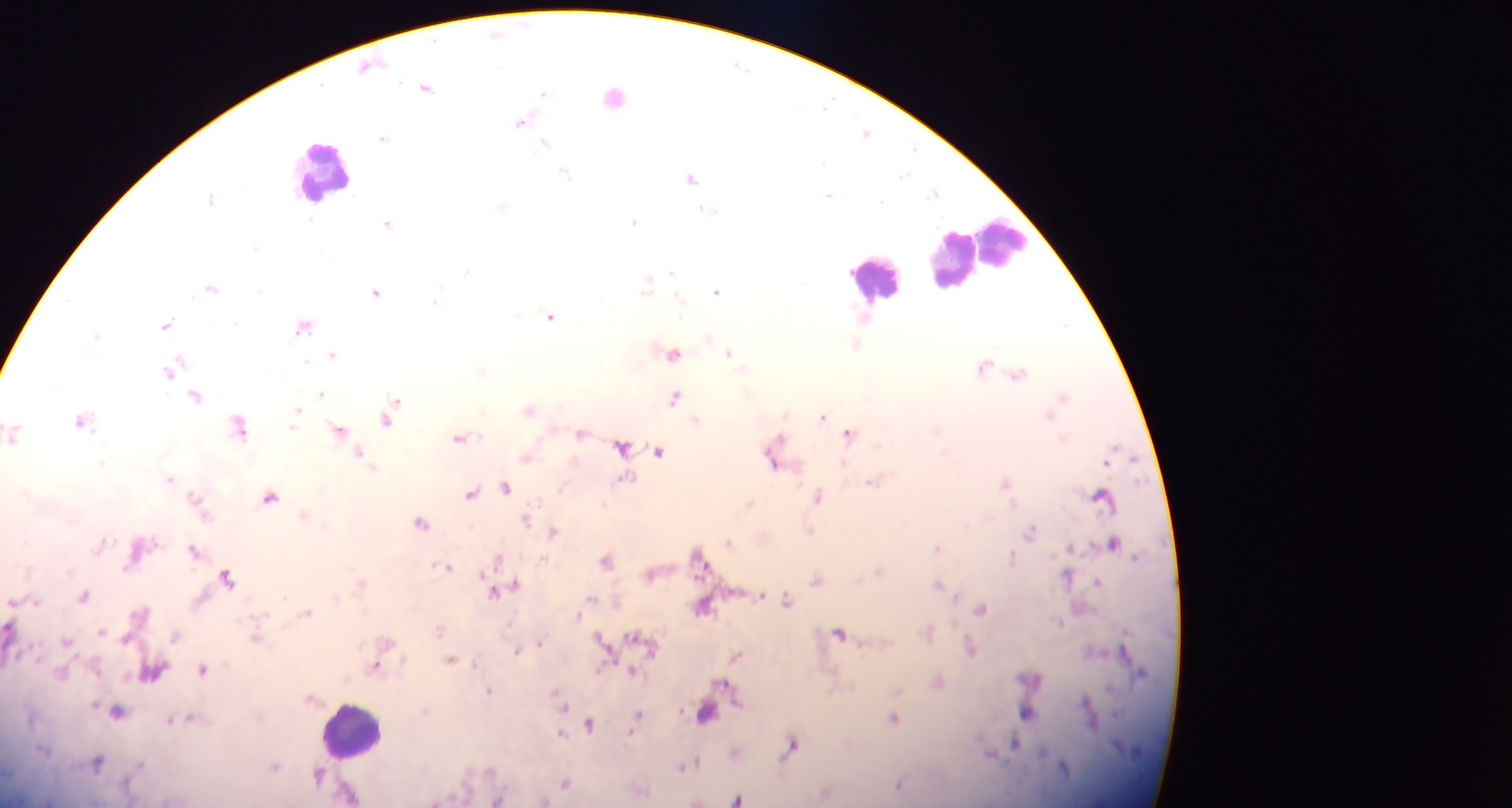
capture: mobile-phone photograph through a microscope
malaria_parasite_locations: 'approximate centers as {x, y} in pixels: {497, 33}, {371, 65}, {426, 87}, {542, 94}, {829, 102}, {523, 121}, {866, 132}, {384, 137}, {546, 143}, {912, 147}, {565, 173}, {906, 177}, {691, 178}, {933, 190}, {829, 194}, {635, 221}, {388, 222}, {643, 286}, {212, 287}, {716, 290}, {374, 292}, {678, 298}, {436, 300}, {516, 315}, {551, 315}, {166, 322}, {1067, 323}, {300, 328}, {857, 345}, {730, 353}, {673, 354}, {334, 355}, {307, 362}, {984, 363}, {174, 367}, {481, 370}, {1019, 373}, {320, 393}, {1065, 395}, {197, 396}, {674, 397}, {530, 408}, {390, 414}, {1049, 414}, {296, 415}, {823, 417}, {82, 422}, {238, 430}, {343, 433}, {581, 434}, {463, 435}, {1065, 436}, {848, 443}, {774, 452}, {526, 457}, {1107, 464}, {845, 468}, {168, 478}, {1142, 478}, {1006, 481}, {873, 482}, {621, 483}, {562, 488}, {271, 495}, {819, 495}, {195, 497}, {605, 504}, {748, 504}, {1014, 505}, {303, 514}, {527, 519}, {554, 530}, {811, 531}, {1032, 531}, {729, 543}, {939, 549}, {1071, 549}, {195, 550}, {697, 553}, {1138, 557}, {496, 558}, {1013, 559}, {449, 566}, {227, 575}, {1070, 578}, {817, 580}, {1101, 581}, {938, 584}, {495, 593}, {86, 596}, {591, 597}, {788, 600}, {618, 601}, {706, 608}, {983, 609}, {309, 610}, {578, 614}, {1061, 621}, {10, 627}, {438, 631}, {598, 633}, {100, 634}, {840, 634}, {176, 635}, {634, 635}, {1123, 635}, {256, 638}, {126, 639}, {542, 641}, {66, 642}, {971, 648}, {516, 651}, {736, 656}, {451, 660}, {375, 666}, {600, 668}, {202, 671}, {632, 671}, {727, 683}, {1110, 689}, {489, 691}, {1087, 692}, {1086, 699}, {101, 707}, {425, 711}, {638, 713}, {707, 713}, {894, 716}, {591, 723}, {563, 734}, {1014, 742}, {791, 745}, {1049, 751}, {696, 759}, {691, 763}, {683, 767}, {1065, 767}, {739, 797}'
country: Ghana
preparation: thick blood smear
image_size: 1512×808 pixels
leukocyte_locations: 'approximate centers as {x, y} in pixels: {322, 163}, {976, 259}, {878, 269}, {348, 727}'
field_of_view: single